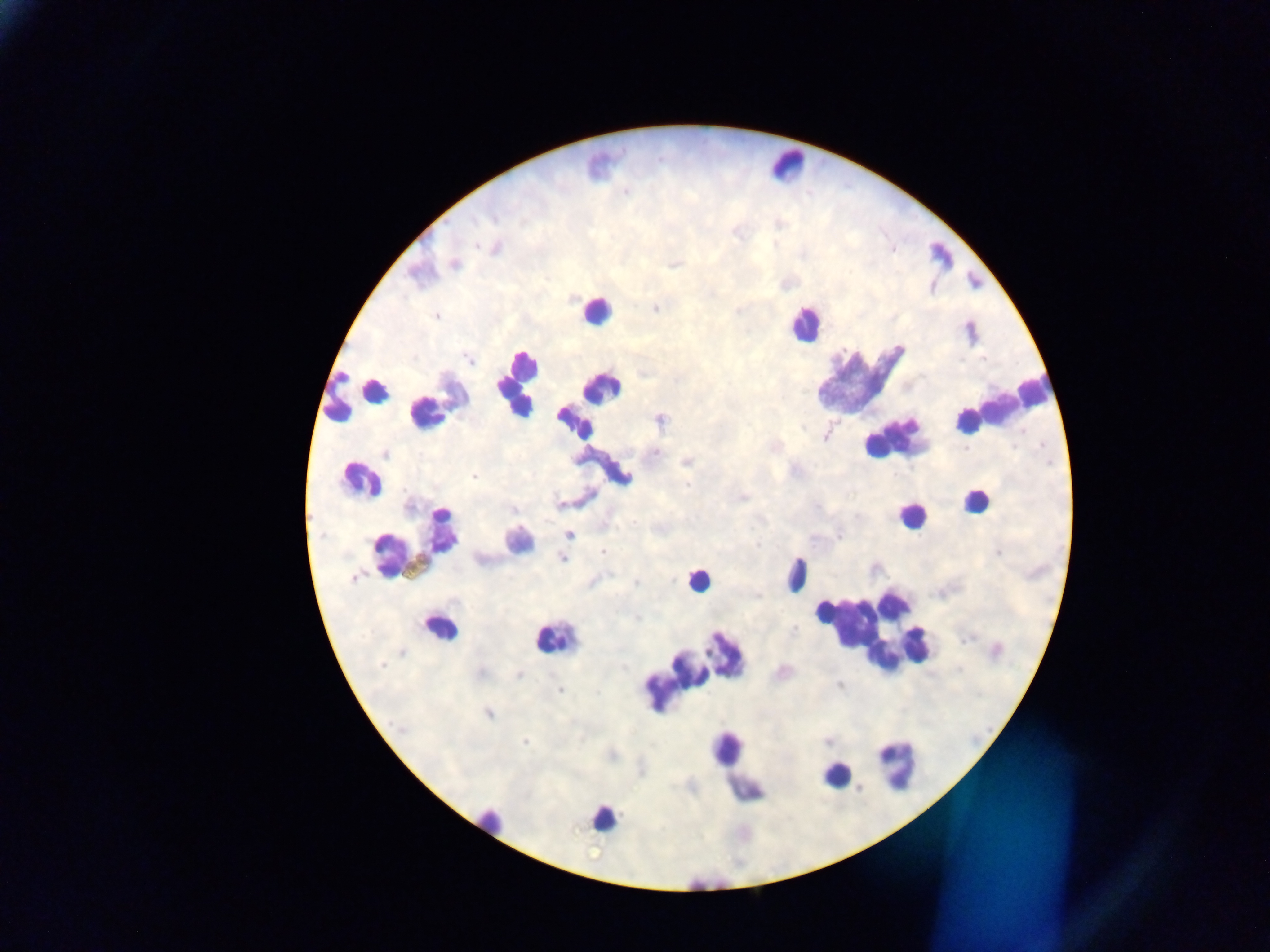 Approximate centers as {x, y} in pixels. Malaria parasite locations: {437, 316}, {385, 453}, {474, 476}, {569, 535}, {603, 552}, {562, 558}, {353, 578}, {519, 675}, {560, 689}, {488, 714}, {524, 742}. Leukocyte locations: {785, 164}, {595, 312}, {804, 324}, {859, 382}, {516, 384}, {355, 391}, {590, 402}, {432, 407}, {996, 408}, {892, 434}, {360, 480}, {975, 503}, {908, 516}, {517, 537}, {420, 542}, {797, 573}, {697, 580}, {441, 627}, {870, 629}, {551, 638}, {693, 667}, {895, 764}, {736, 769}, {835, 775}, {604, 818}, {492, 824}. Image is 1270×952 pixels. Thick blood film. Photographed through a microscope with a mobile-phone camera. One field of view. Sample from Ghana.